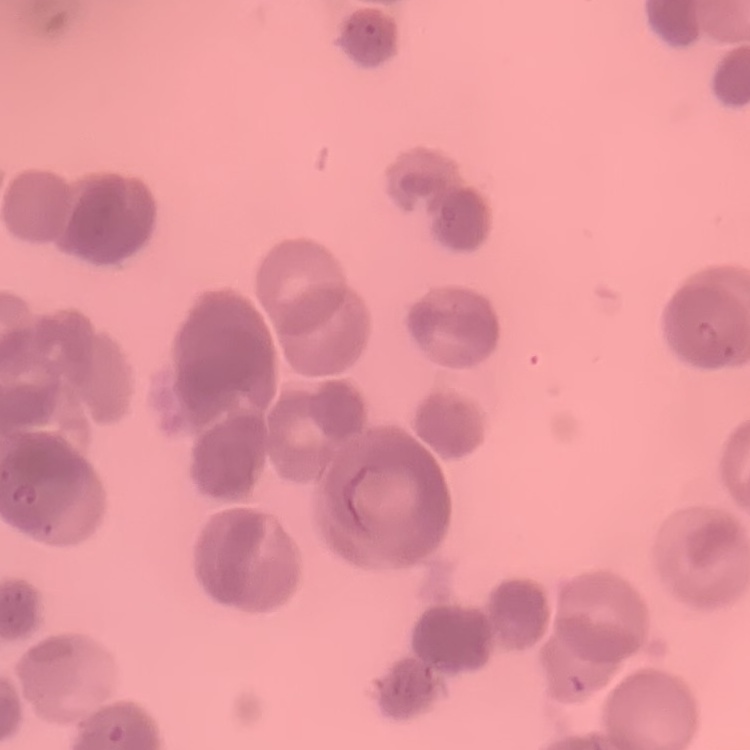
The erythrocytes exhibit rouleaux formation. Square crop of a larger photomicrograph. Thin blood smear. Field's or Giemsa stain.